Describe the morphology of the red blood cells.
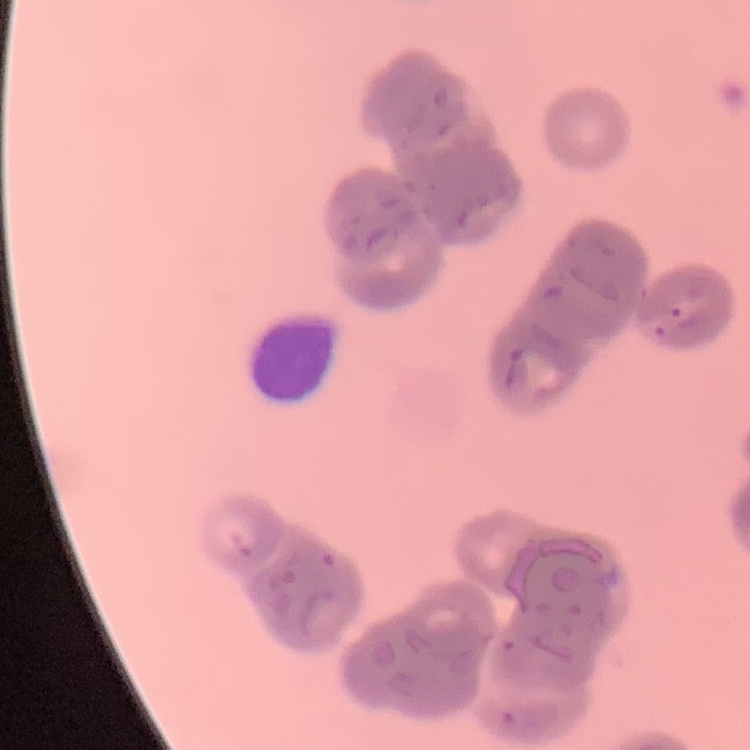

Rouleaux formation.

{
  "stain": "Field's or Giemsa",
  "preparation": "thin blood film",
  "image_type": "one tile cut from a larger photomicrograph"
}